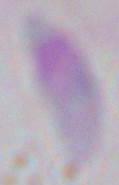
Captured at 1000x magnification. Photomicrograph. Toxoplasma gondii is shown.